Look for parasitized red blood cells.
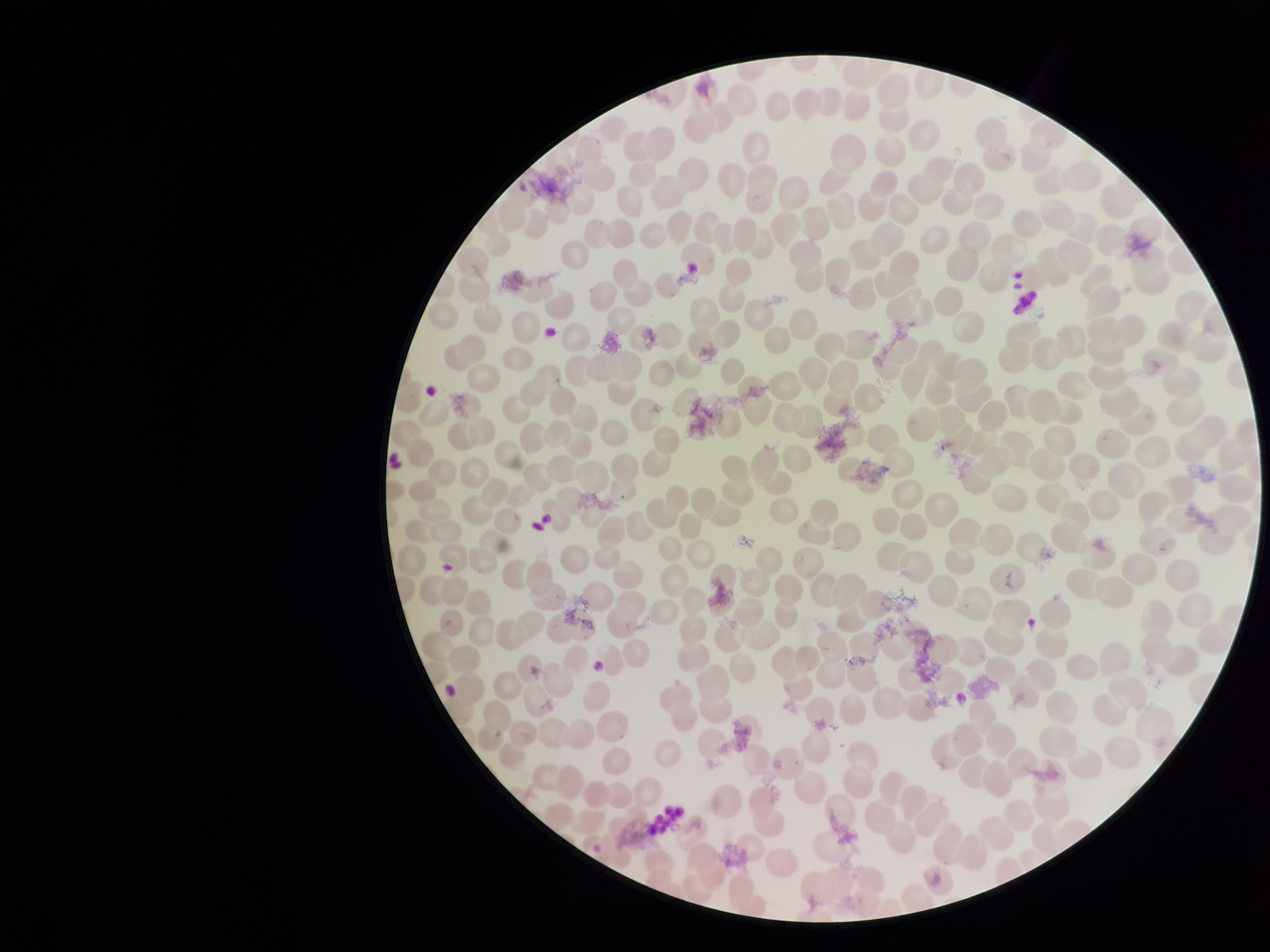

None seen.

parasitized_red_blood_cell_count: 0
image_size: 1270×952 pixels
capture: smartphone photograph through the microscope eyepiece
red_blood_cell_count: 218
field_of_view: single
patient_malaria_status: negative
stain: Giemsa
preparation: thin